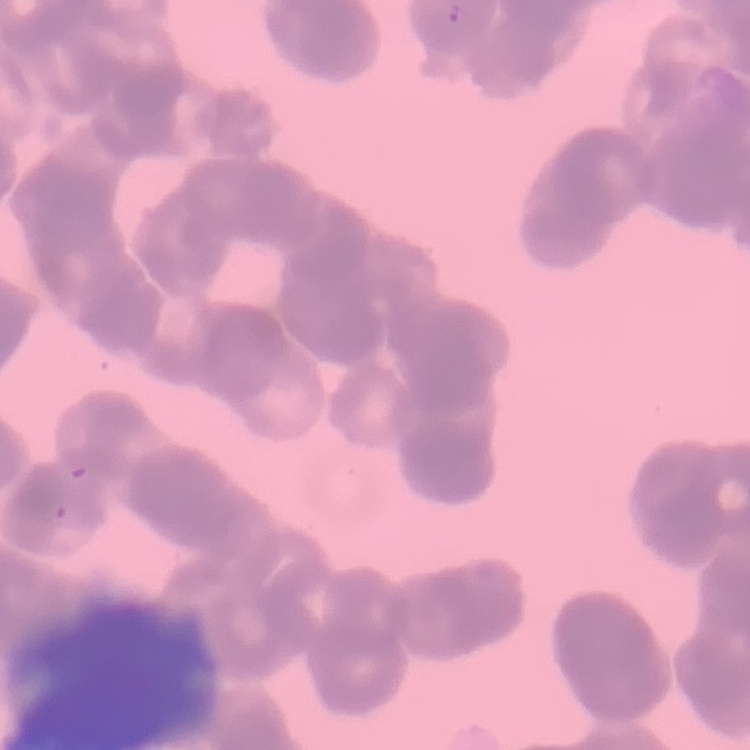
The red blood cells show rouleaux formation. Stained with either Field's or Giemsa. Thin blood film. One tile cut from a larger photomicrograph.